Locate every Plasmodium parasite.
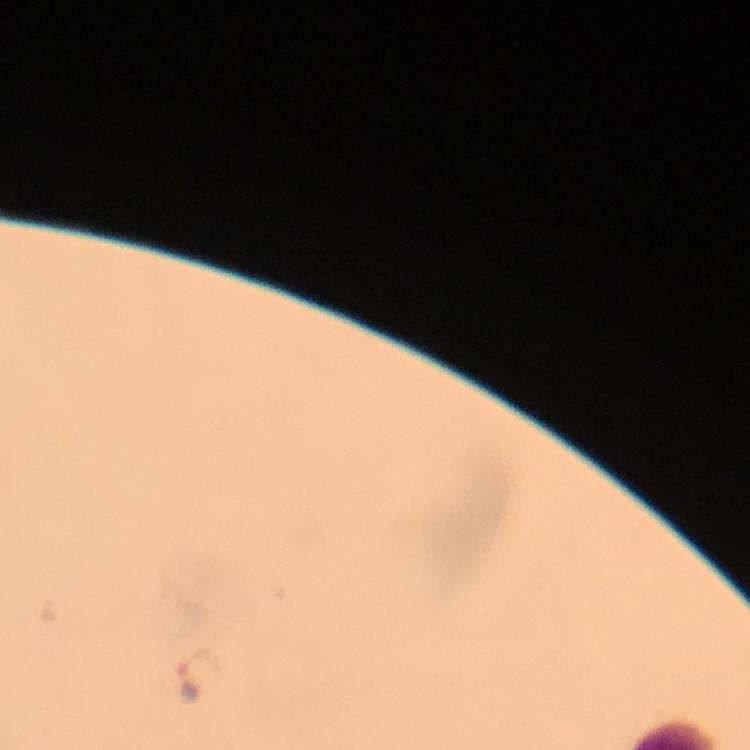

Approximate centers as (x, y) in pixels.
Plasmodium parasites: (199, 676).

Giemsa stain. A crop from one field of view. Image is 750×750 pixels. 100x magnification. Immersion oil was used. Photographed with a smartphone mounted on the microscope. From a malaria diagnostic workup. Thick blood film.